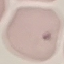 Malaria status: uninfected. Giemsa-stained preparation. Thin blood smear. Acquired by smartphone through the microscope eyepiece. Cell patch, automatically extracted from a larger field of view and resized to 64 × 64 pixels.